Give the extent of all uninfected red blood cells.
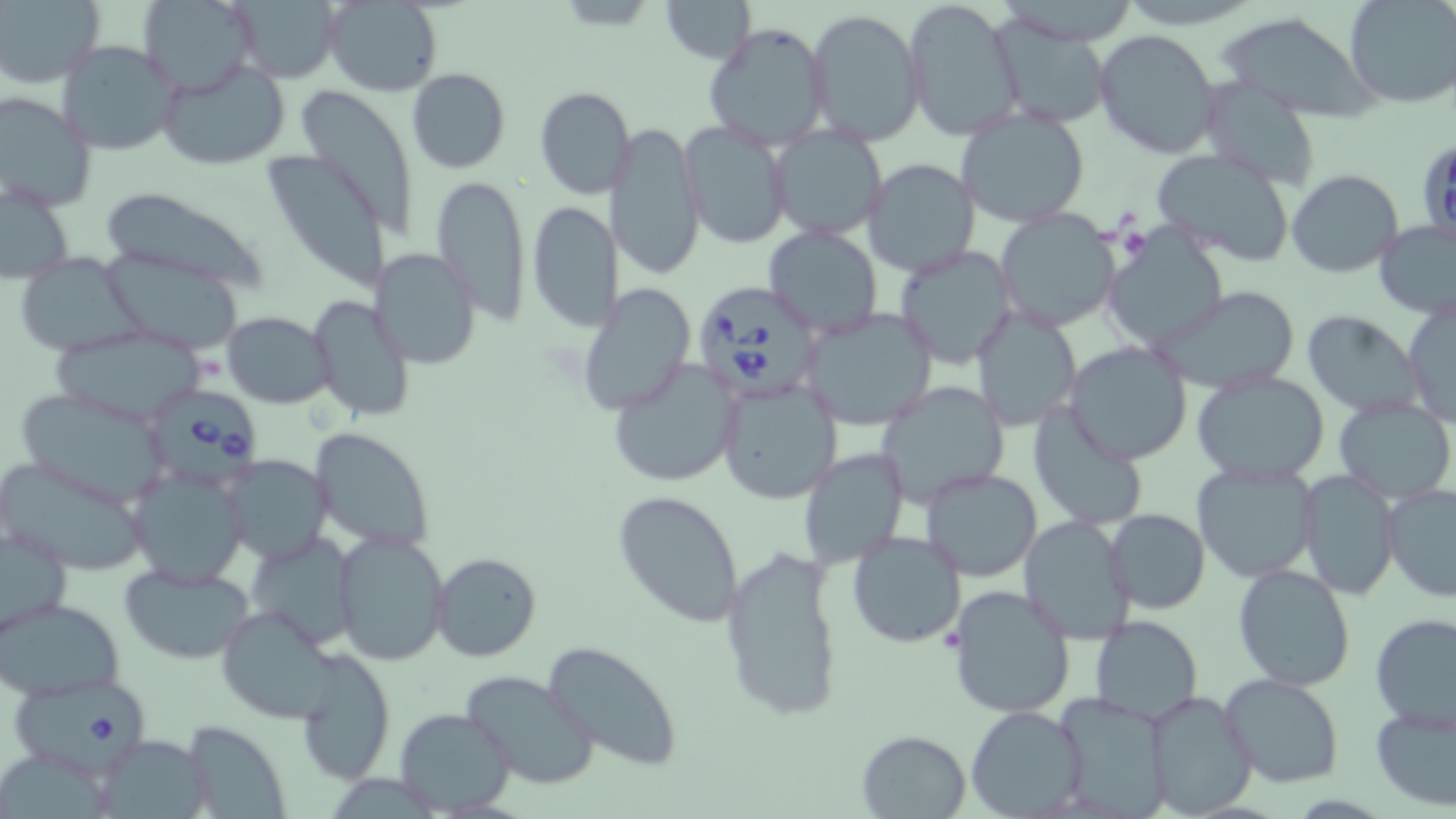
Approximate bounding boxes as (x1, y1, x2, y2) in pixels.
Uninfected red blood cells: (137, 0, 258, 94), (223, 0, 342, 84), (322, 0, 442, 94), (658, 0, 755, 64), (1344, 0, 1456, 108), (1, 1, 104, 87), (901, 1, 1020, 139), (806, 8, 926, 146), (984, 14, 1114, 129), (1218, 15, 1380, 120), (701, 21, 833, 152), (1094, 29, 1221, 157), (55, 39, 183, 155), (157, 60, 291, 170), (406, 67, 510, 174), (1198, 74, 1322, 192), (534, 86, 636, 200), (298, 89, 417, 235), (0, 93, 96, 213), (955, 106, 1091, 229), (680, 120, 793, 249), (607, 121, 706, 281), (768, 125, 889, 241), (263, 148, 391, 291), (1153, 148, 1297, 265), (863, 158, 979, 276), (1285, 169, 1402, 278), (430, 173, 532, 322), (1, 180, 75, 285), (97, 187, 275, 290), (527, 201, 620, 332), (994, 209, 1120, 332), (1373, 219, 1456, 319), (760, 225, 884, 337), (1102, 228, 1227, 351), (894, 245, 1017, 369), (370, 249, 480, 369), (101, 252, 241, 352), (13, 254, 144, 356), (577, 282, 696, 414), (1155, 287, 1302, 392), (307, 293, 415, 424), (1402, 297, 1455, 428), (972, 304, 1082, 431), (798, 305, 940, 431), (222, 311, 334, 407), (1302, 312, 1424, 418), (52, 325, 211, 427), (1064, 341, 1192, 464), (606, 357, 744, 489), (1192, 370, 1330, 484), (716, 376, 841, 505), (879, 381, 1008, 503), (15, 388, 173, 506), (1333, 397, 1455, 503), (1029, 403, 1150, 531), (310, 427, 435, 552), (796, 447, 908, 569), (0, 454, 151, 574), (222, 455, 333, 564), (1191, 459, 1319, 582), (129, 465, 247, 588), (919, 467, 1040, 582), (1298, 470, 1401, 600), (1381, 485, 1456, 601), (613, 490, 745, 627), (1105, 508, 1211, 613), (1017, 515, 1139, 643), (1, 525, 73, 637), (845, 529, 967, 649), (245, 532, 357, 649), (334, 533, 449, 665), (721, 544, 843, 723), (431, 552, 542, 662), (119, 562, 256, 664), (1232, 563, 1356, 692), (947, 583, 1078, 720), (0, 597, 125, 701), (215, 604, 335, 723), (1370, 613, 1456, 731), (1088, 615, 1203, 725), (542, 641, 684, 770), (295, 650, 397, 787), (460, 670, 600, 790), (1219, 675, 1345, 788), (1143, 689, 1260, 817), (1049, 691, 1176, 818), (1370, 704, 1456, 812), (966, 705, 1088, 817), (395, 707, 517, 815), (183, 719, 293, 819), (856, 729, 972, 817), (94, 732, 214, 819).

slide-level diagnosis = Babesia divergens
stain = May-Grünwald-Giemsa
modality = optical microscopy
preparation = thin blood smear
magnification = 1000x
image size = 1456×819 pixels
Babesia divergens-infected red blood cell locations = approximate bounding boxes as (x1, y1, x2, y2) in pixels: (1420, 141, 1456, 244), (691, 284, 825, 405), (152, 384, 267, 491), (9, 675, 155, 773)
field of view = single